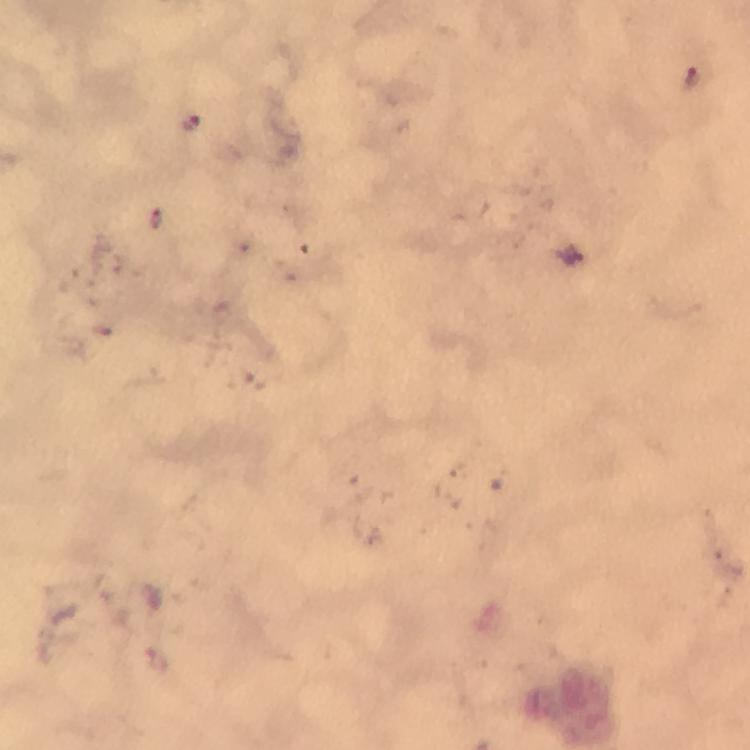 Approximate centers as [x, y] in pixels. Malaria parasite locations: [692, 75], [159, 220]. Photographed with a smartphone mounted on the microscope. From a diagnostic examination for malaria. Giemsa-stained preparation. Image is 750×750 pixels. At 100x magnification. Thick blood film. Immersion oil applied. Cropped region of a single field of view.